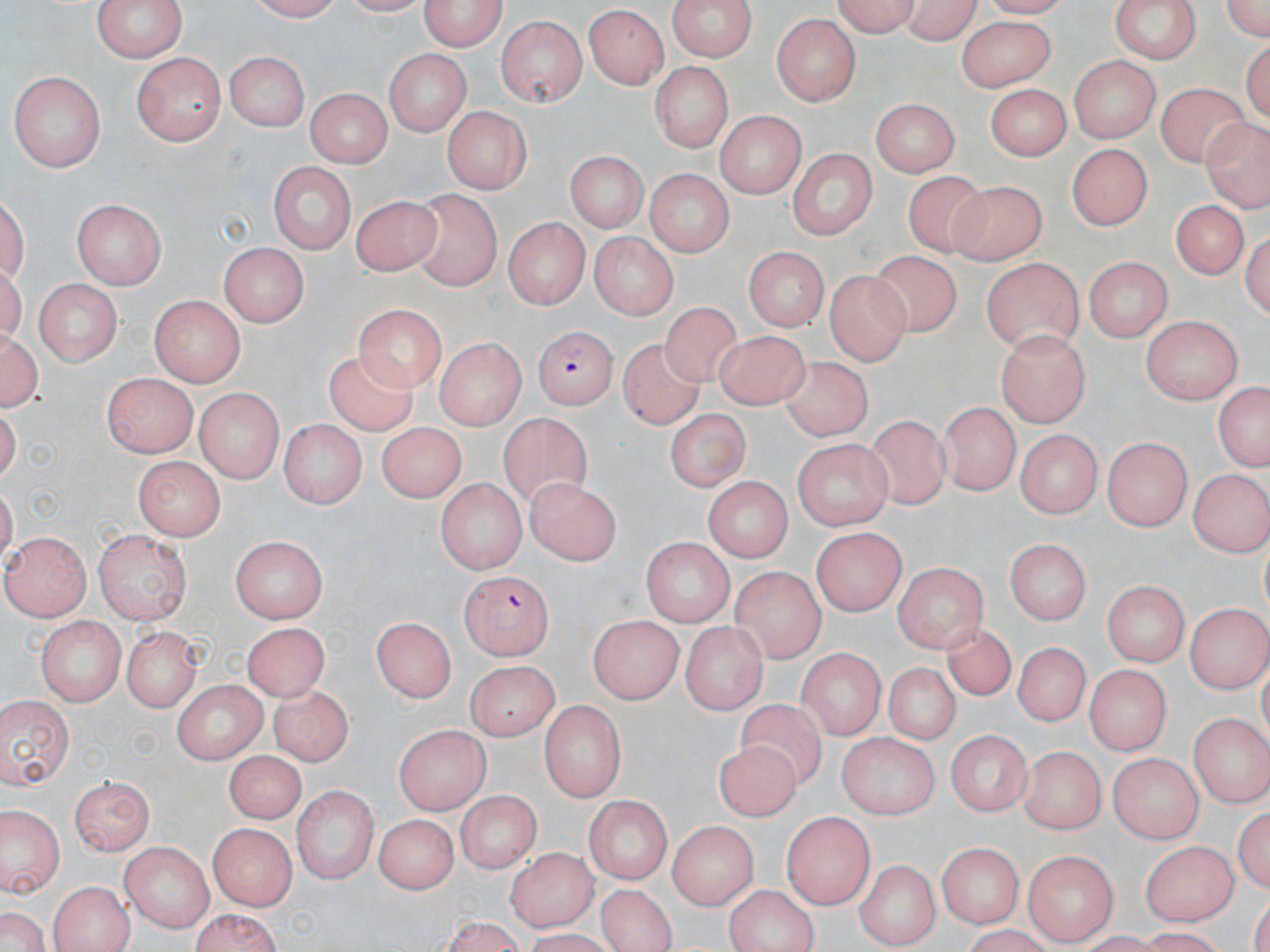

Summary:
  - Coordinate format: approximate bounding boxes as (x1,y1)-(x2,y2) corner pairs in pixels
  - Plasmodium falciparum-infected red blood cell locations: (531,325)-(620,409), (458,569)-(550,659)
  - Uninfected red blood cell locations: (94,0)-(184,64), (242,0)-(349,23), (420,0)-(505,52), (668,0)-(757,60), (829,0)-(922,35), (900,0)-(986,45), (1216,0)-(1270,48), (1110,1)-(1200,66), (583,6)-(670,90), (773,12)-(860,105), (497,15)-(588,108), (952,16)-(1058,87), (225,49)-(306,130), (387,49)-(471,136), (134,53)-(225,146), (1067,56)-(1161,141), (651,61)-(732,156), (9,71)-(106,171), (986,82)-(1070,161), (1155,84)-(1258,171), (305,89)-(393,166), (871,97)-(958,177), (441,106)-(530,195), (715,110)-(807,198), (1201,116)-(1269,207), (1067,142)-(1155,230), (788,145)-(878,238), (563,150)-(651,231), (266,160)-(353,251), (642,169)-(734,258), (904,172)-(995,260), (948,180)-(1047,262), (411,189)-(501,287), (351,193)-(443,278), (74,198)-(168,287), (1170,200)-(1249,281), (502,217)-(588,311), (589,231)-(679,320), (219,243)-(308,327), (739,245)-(833,330), (873,247)-(959,340), (1085,255)-(1172,343), (976,258)-(1087,351), (824,272)-(908,366), (37,279)-(121,368), (149,296)-(244,387), (660,300)-(753,392), (353,302)-(444,388), (1141,315)-(1246,406), (2,326)-(42,416), (714,327)-(809,411), (996,328)-(1089,428), (433,338)-(527,426), (621,339)-(709,430), (325,347)-(423,438), (778,353)-(880,449), (105,378)-(196,457), (1211,384)-(1270,473), (193,388)-(286,483), (940,396)-(1021,497), (664,407)-(749,493), (496,413)-(596,516), (276,419)-(368,507), (869,419)-(959,517), (373,422)-(469,502), (1017,431)-(1101,516), (1103,438)-(1193,530), (790,442)-(893,531), (133,456)-(224,539), (1186,468)-(1267,555), (528,475)-(624,564), (434,478)-(528,572), (705,480)-(790,563), (112,484)-(213,610), (811,526)-(904,614), (6,531)-(91,620), (98,531)-(193,623), (231,535)-(327,623), (643,536)-(733,627), (1006,538)-(1090,622), (893,561)-(989,648), (733,568)-(826,664), (1100,580)-(1191,667), (1118,596)-(1261,677), (1185,601)-(1268,695), (36,615)-(122,708), (373,615)-(459,701), (589,615)-(686,702), (241,620)-(332,703), (679,621)-(770,711), (938,621)-(1027,700), (119,627)-(205,710), (1009,641)-(1094,726), (798,650)-(884,740), (463,659)-(560,739), (884,663)-(963,748), (1088,667)-(1167,755), (174,678)-(268,763), (270,679)-(354,766), (1,696)-(75,791), (731,698)-(835,789), (540,699)-(627,800), (1190,712)-(1270,808), (393,722)-(487,813), (946,730)-(1032,819), (838,732)-(937,816), (714,740)-(801,817), (1020,746)-(1105,834), (225,752)-(301,825), (1108,754)-(1199,840), (71,772)-(155,856), (297,785)-(377,882), (453,789)-(542,873), (583,796)-(674,882), (1235,799)-(1269,902), (3,810)-(59,897), (374,812)-(457,894), (779,813)-(876,906), (662,820)-(758,917), (207,824)-(293,911), (938,841)-(1022,931), (1141,842)-(1238,926), (120,843)-(212,931), (503,848)-(596,932), (1024,848)-(1118,942), (853,860)-(938,948), (48,879)-(134,952), (588,881)-(681,952), (725,885)-(820,952), (0,903)-(53,952), (183,911)-(286,951)
  - Slide-level diagnosis: Plasmodium falciparum
  - Image size: 1270×952 pixels
  - Modality: light microscopy
  - Magnification: 1000x
  - Field of view: one of a larger specimen
  - Preparation: thin blood smear
  - Stain: May-Grünwald-Giemsa